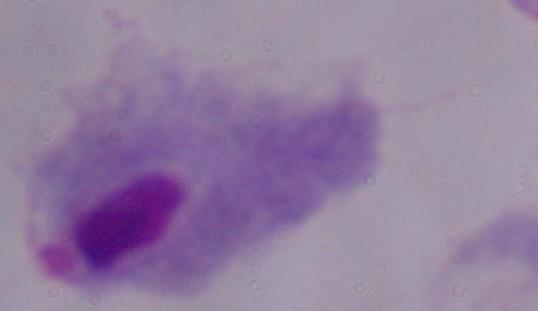
Summary:
  - Modality: photomicrograph
  - Magnification: 1000x
  - Identification: trichomonad